Report the malaria status of this cell.
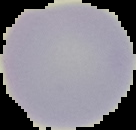

Uninfected.

image type = cell region segmented out of the field of view; surrounding area masked to black
image size = 136×130 pixels
preparation = thin blood film